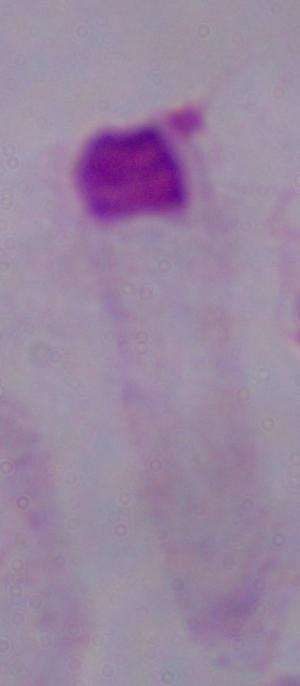

identification = trichomonad
magnification = 1000x
modality = photomicrograph